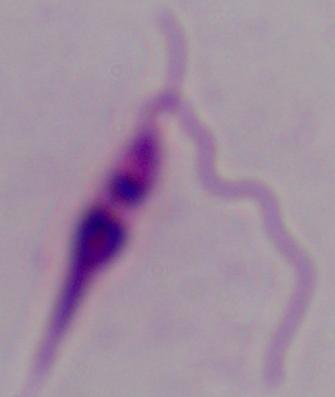

Summary:
  - Modality: photomicrograph
  - Magnification: 1000x
  - Identification: Leishmania